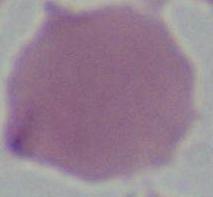

1000x magnification. An erythrocyte is shown. Photomicrograph.